Classify this cell by malaria status.
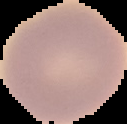
It is uninfected.

Summary:
  - Image type: segmented cell region with the area outside set to black
  - Preparation: thin blood film
  - Image size: 127×124 pixels